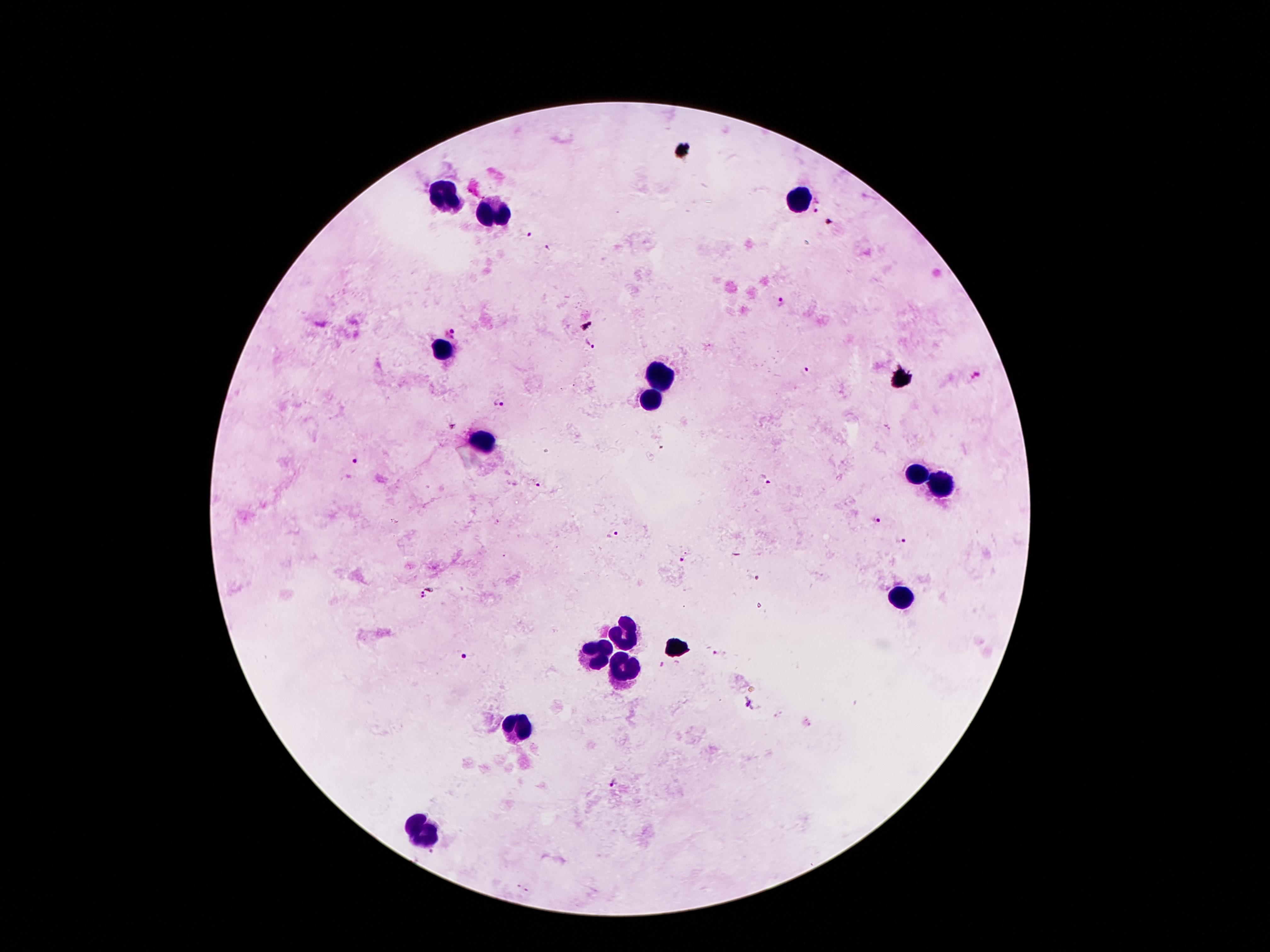
Approximate object centers, in pixels from the top-left corner. Malaria parasite locations: (x=816, y=206), (x=831, y=221), (x=526, y=235), (x=549, y=250), (x=780, y=300), (x=453, y=333), (x=589, y=344), (x=806, y=371), (x=978, y=377), (x=499, y=401), (x=354, y=460), (x=765, y=481), (x=538, y=485), (x=874, y=520), (x=613, y=535), (x=900, y=539), (x=685, y=559), (x=755, y=577), (x=423, y=594), (x=464, y=656), (x=749, y=703), (x=614, y=783). Leukocyte locations: (x=447, y=195), (x=801, y=200), (x=498, y=214), (x=444, y=351), (x=658, y=377), (x=651, y=401), (x=483, y=443), (x=916, y=474), (x=943, y=486), (x=905, y=598), (x=625, y=633), (x=598, y=656), (x=622, y=668), (x=521, y=727), (x=429, y=832). Photographed through the microscope eyepiece with a smartphone camera. 100x magnification. Giemsa-stained preparation. Image is 1270×952 pixels. Patient malaria status: infected with Plasmodium falciparum. Thick peripheral-blood smear. Single field of view.